Name the parasite shown.
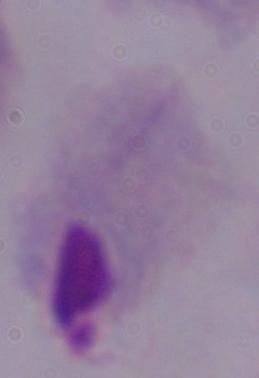
This is a trichomonad.

Summary:
  - Magnification: 1000x
  - Modality: micrograph